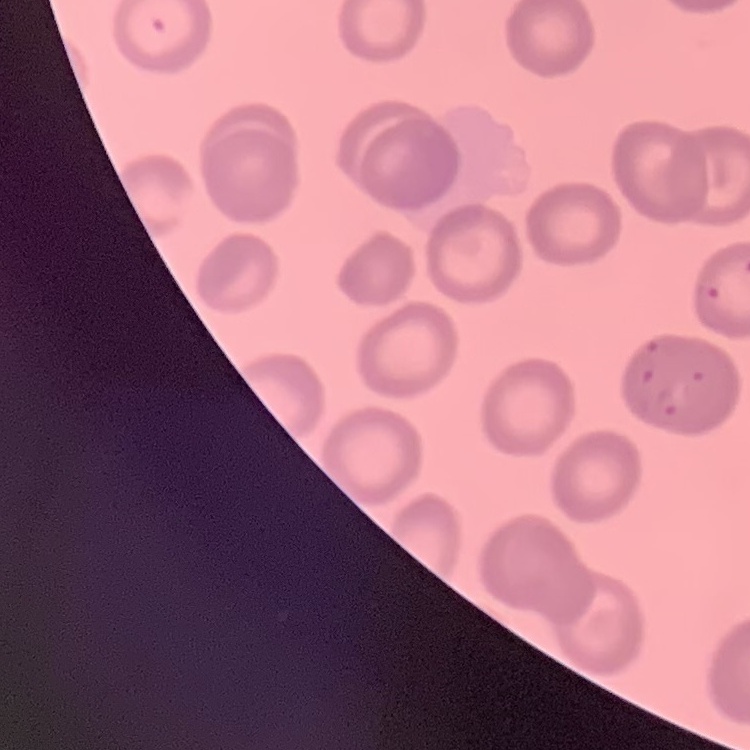

The red blood cells show no rouleaux formation. Thin blood smear. Stained with either Field's or Giemsa. Square crop of a larger photomicrograph.